Assess this cell for malaria.
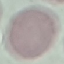
It is uninfected.

Thin smear of blood. Giemsa stain. Photographed with a smartphone camera at the microscope eyepiece. Cell patch, automatically extracted from a larger field of view and resized to 64 × 64 pixels.